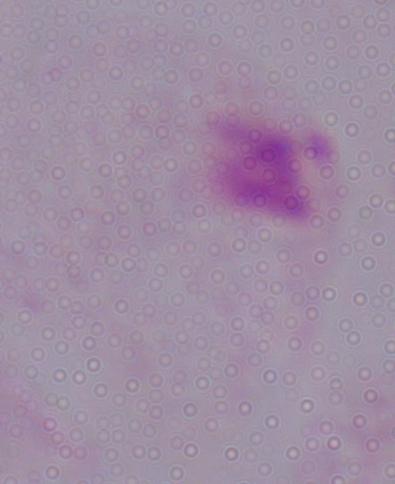

Summary:
  - Modality: photomicrograph
  - Magnification: 1000x
  - Identification: trichomonad